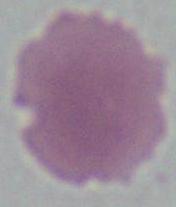

Micrograph. An erythrocyte is shown. Captured at 1000x magnification.